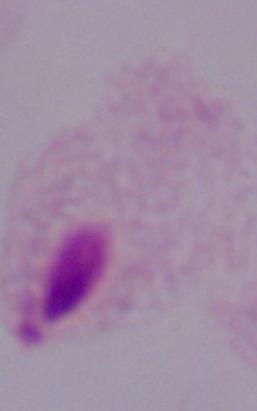

magnification: 1000x
modality: micrograph
identification: trichomonad